Assess the morphology of the erythrocytes.
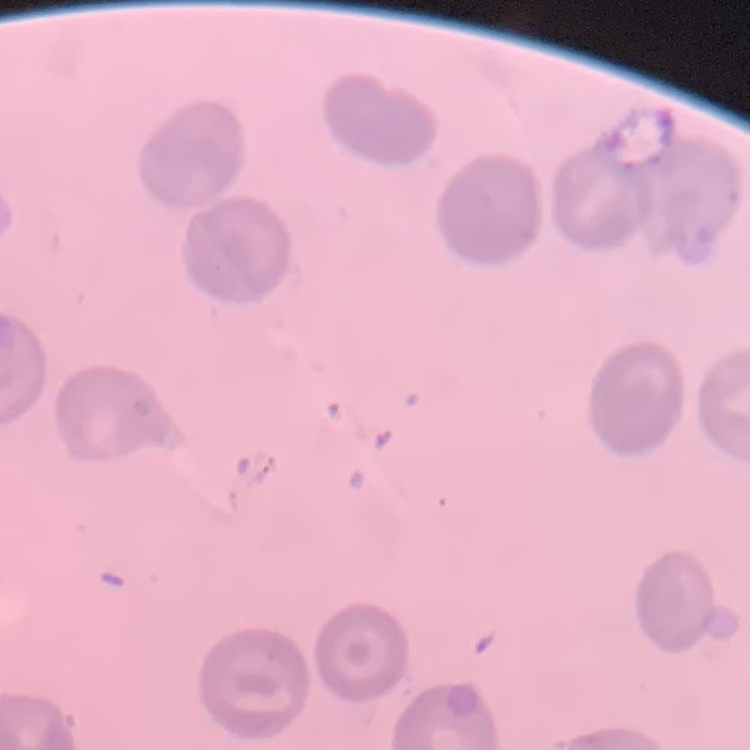

They show no rouleaux formation.

Stained with either Field's or Giemsa. Thin peripheral smear. Square crop of a larger photomicrograph.